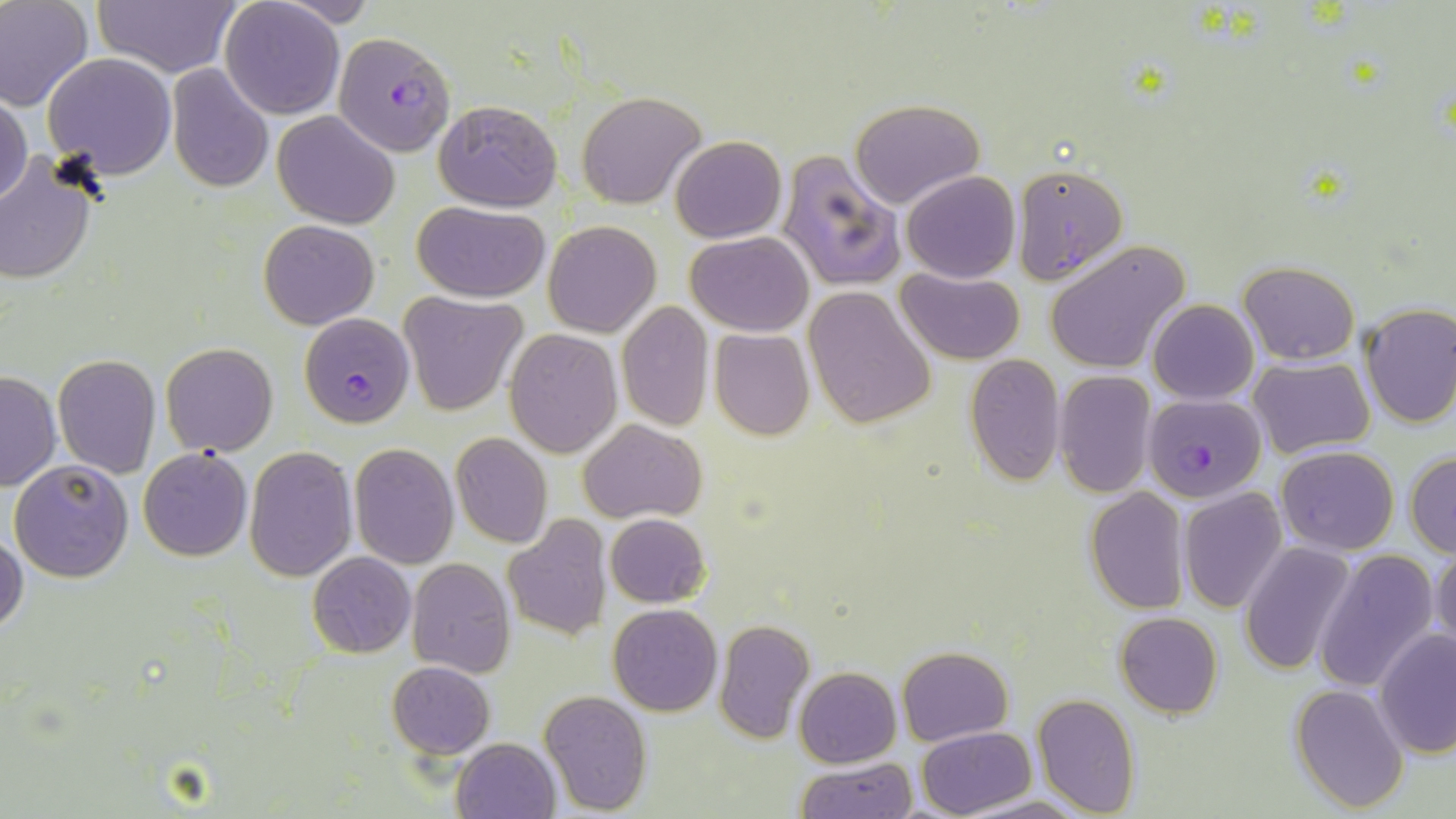

Summary:
  - Coordinate format: approximate bounding boxes as (x1,y1)-(x2,y2) corner pairs in pixels
  - Plasmodium falciparum-infected red blood cell locations: (329,34)-(454,163), (298,312)-(415,428), (1140,392)-(1266,502)
  - Uninfected red blood cell locations: (0,0)-(94,111), (89,0)-(241,76), (220,0)-(345,118), (43,52)-(176,178), (168,64)-(274,194), (0,87)-(31,207), (577,92)-(706,209), (849,97)-(987,208), (433,98)-(562,210), (273,111)-(399,227), (670,135)-(786,243), (778,149)-(904,292), (0,152)-(100,285), (1012,163)-(1127,285), (900,171)-(1020,282), (412,201)-(550,302), (258,219)-(380,328), (543,220)-(660,338), (685,231)-(814,337), (1044,241)-(1188,373), (1238,261)-(1359,365), (896,267)-(1024,363), (804,287)-(935,430), (401,292)-(527,415), (1149,299)-(1258,403), (617,301)-(713,432), (1358,303)-(1456,428), (709,329)-(815,441), (505,330)-(621,457), (161,344)-(277,457), (52,352)-(160,478), (964,355)-(1065,486), (1249,356)-(1374,458), (1,371)-(60,492), (1054,371)-(1157,497), (579,419)-(706,523), (451,433)-(552,547), (350,442)-(458,568), (1277,445)-(1400,554), (244,446)-(357,582), (138,448)-(252,562), (1406,451)-(1456,557), (9,458)-(133,583), (1178,487)-(1287,613), (1084,488)-(1189,614), (605,512)-(710,607), (502,517)-(612,642), (1,529)-(26,636), (1240,543)-(1358,676), (1430,543)-(1456,663), (1313,548)-(1439,693), (307,552)-(416,658), (405,558)-(516,677), (608,603)-(723,716), (1115,612)-(1222,719), (713,619)-(815,744), (1375,630)-(1456,758), (898,646)-(1013,745), (387,661)-(494,759), (794,667)-(902,767), (1290,682)-(1409,812), (537,690)-(652,814), (1031,692)-(1140,816), (917,726)-(1036,817), (451,737)-(560,819), (794,757)-(916,819), (956,791)-(1084,819)
  - Slide-level diagnosis: Plasmodium falciparum
  - Field of view: single
  - Preparation: thin blood smear
  - Magnification: 1000x
  - Stain: May-Grünwald-Giemsa
  - Modality: light microscopy
  - Image size: 1456×819 pixels